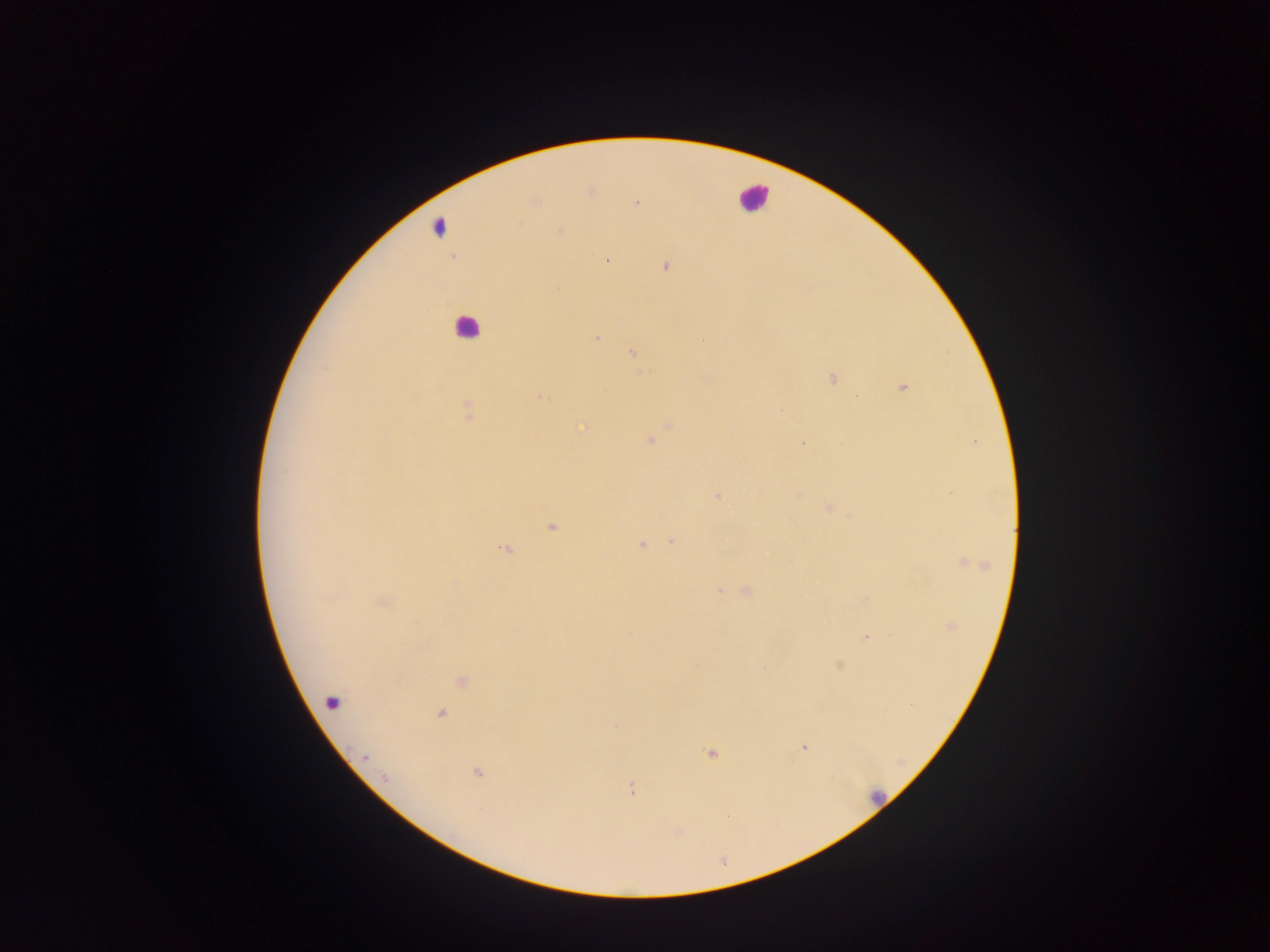

{
  "leukocyte_locations": "approximate centers as (x, y) in pixels: (752, 196), (437, 226), (466, 327), (332, 701), (875, 797)",
  "capture": "mobile-phone photograph through a microscope",
  "field_of_view": "single",
  "image_size": "1270×952 pixels",
  "malaria_parasite_locations": "approximate centers as (x, y) in pixels: (636, 203), (519, 223), (559, 231), (606, 260), (665, 267), (558, 288), (596, 337), (632, 352), (325, 368), (833, 378), (902, 387), (542, 397), (467, 409), (650, 440), (803, 443), (284, 472), (951, 493), (717, 496), (829, 508), (552, 527), (671, 541), (641, 545), (507, 549), (967, 563), (719, 590), (747, 590), (951, 626), (630, 634), (866, 637), (764, 668), (911, 705), (441, 713), (804, 747), (711, 754), (365, 756), (478, 773), (385, 778), (631, 788)",
  "country": "Ghana",
  "preparation": "thick blood film"
}